State the blood parasite species.
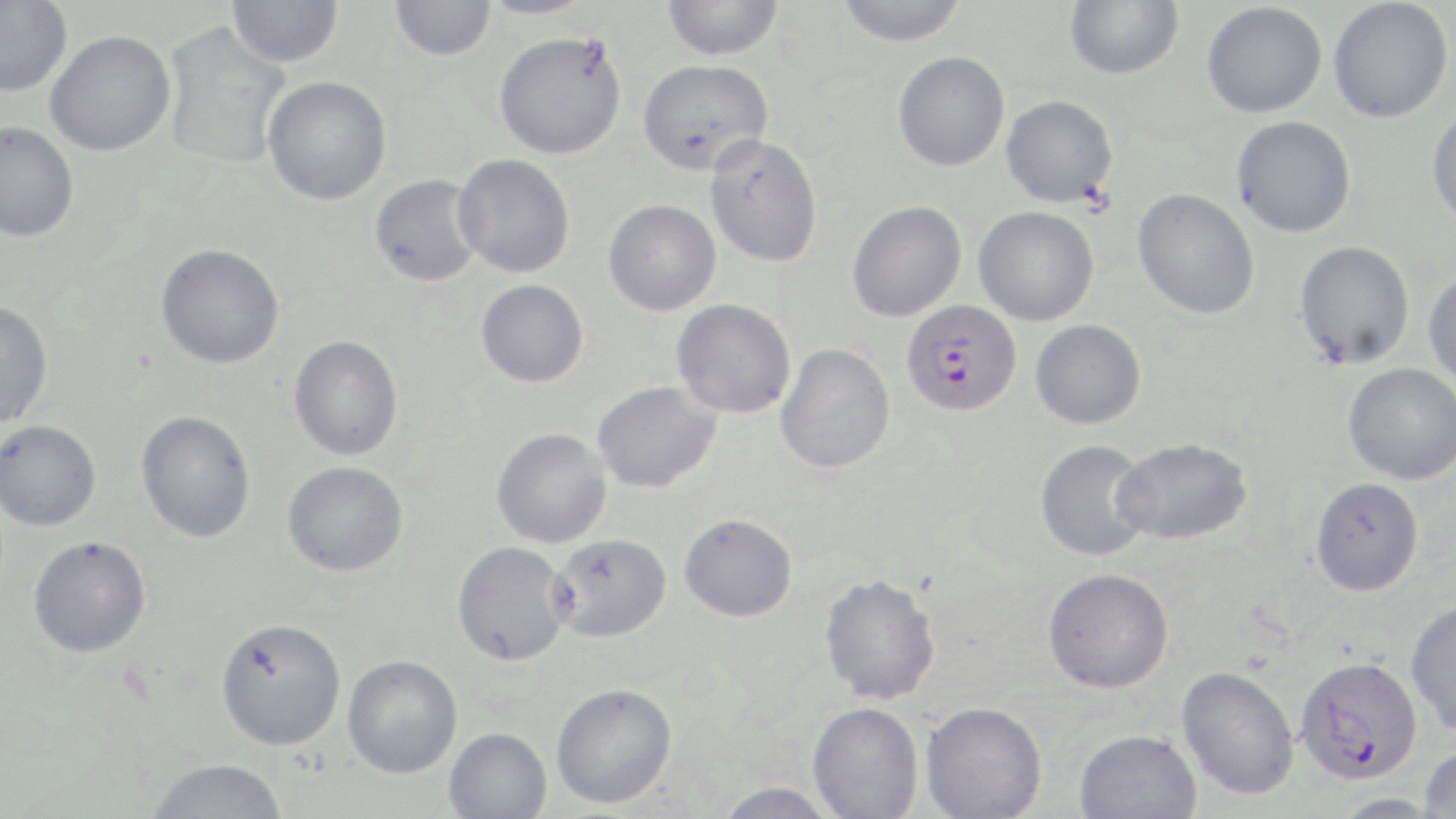
Plasmodium falciparum.

Approximate bounding boxes as [x1, y1, x2, y2] in pixels. Uninfected red blood cell locations: [227, 0, 343, 67], [475, 0, 595, 19], [835, 0, 968, 47], [1065, 0, 1183, 80], [1328, 0, 1453, 123], [0, 1, 73, 98], [390, 1, 496, 61], [662, 1, 784, 60], [1202, 2, 1327, 118], [162, 24, 290, 168], [44, 30, 175, 157], [493, 31, 627, 159], [893, 51, 1010, 171], [638, 58, 773, 176], [262, 76, 392, 205], [1000, 95, 1118, 208], [1427, 105, 1456, 228], [1232, 116, 1356, 238], [0, 121, 79, 242], [704, 134, 823, 268], [453, 154, 575, 278], [369, 174, 484, 287], [1132, 188, 1259, 319], [603, 200, 721, 316], [846, 200, 967, 322], [973, 206, 1099, 326], [1294, 240, 1415, 370], [155, 243, 284, 369], [1423, 271, 1456, 391], [476, 279, 588, 388], [671, 299, 796, 418], [0, 300, 53, 429], [1030, 319, 1146, 429], [288, 335, 403, 461], [775, 343, 895, 474], [1342, 363, 1456, 485], [592, 381, 721, 493], [135, 410, 256, 542], [0, 421, 101, 531], [491, 428, 612, 549], [1113, 437, 1253, 545], [1035, 439, 1154, 562], [282, 461, 408, 577], [1310, 477, 1424, 596], [679, 513, 798, 621], [549, 534, 672, 642], [28, 536, 151, 657], [451, 542, 573, 666], [1042, 568, 1174, 694], [819, 573, 941, 704], [1406, 600, 1456, 736], [215, 617, 346, 750], [342, 654, 463, 778], [1176, 665, 1299, 800], [551, 682, 678, 809], [808, 701, 924, 819], [921, 701, 1047, 819], [444, 727, 552, 819], [1074, 729, 1202, 819], [1419, 744, 1456, 817], [147, 758, 288, 818], [712, 782, 839, 819], [1330, 793, 1444, 818]. Plasmodium falciparum-infected red blood cell locations: [901, 299, 1021, 416], [1294, 655, 1424, 785]. Thin blood smear. May-Grünwald-Giemsa-stained preparation. One field of a larger specimen. Image is 1456×819 pixels. Light microscopy. 1000x magnification.